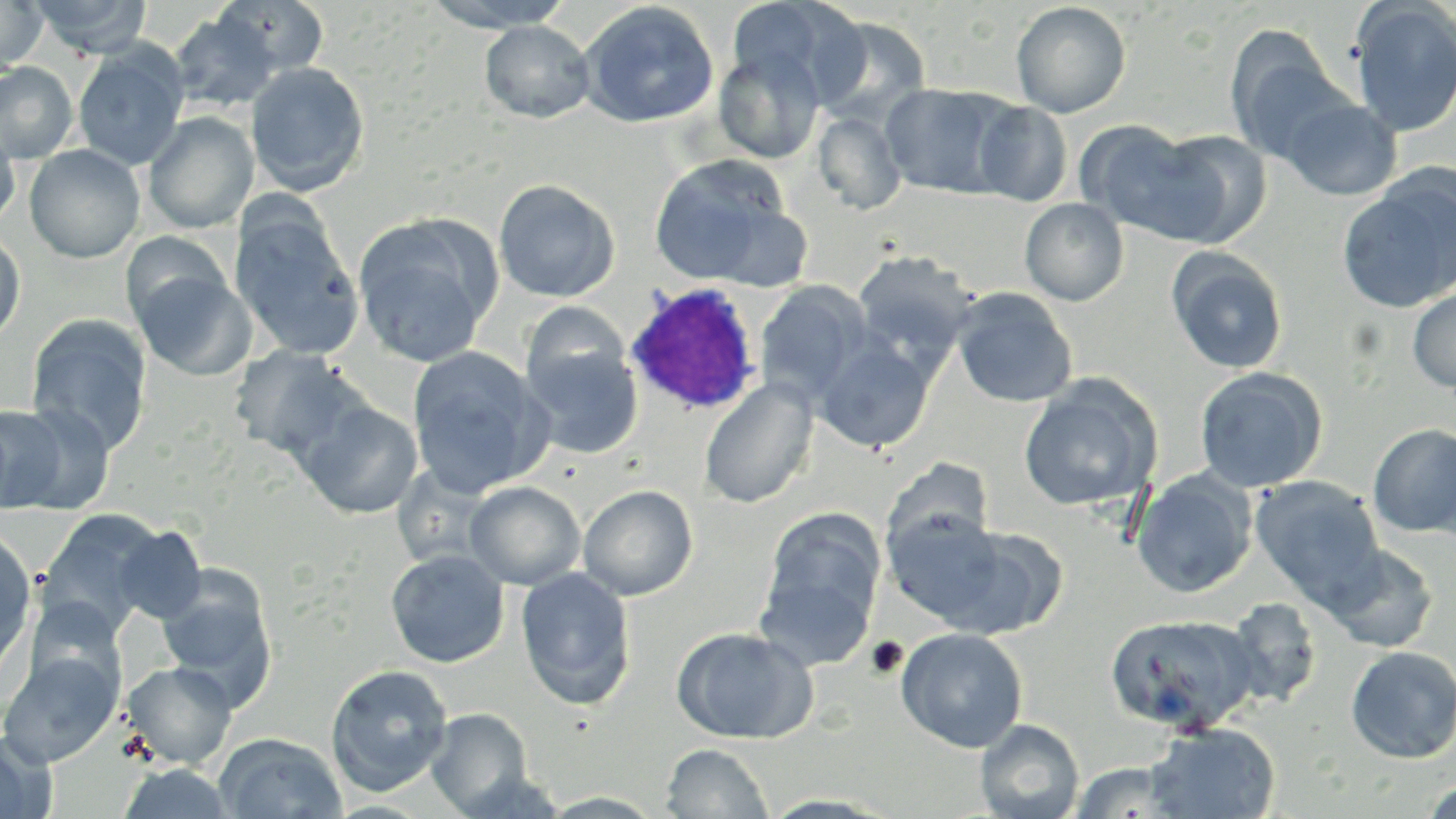
slide_level_diagnosis: Plasmodium ovale
image_size: 1456×819 pixels
uninfected_red_blood_cell_locations: 'approximate bounding boxes as (x1,y1)-(x2,y2) corner pairs in pixels: (30,0)-(152,58), (215,0)-(329,78), (426,0)-(573,31), (727,0)-(840,93), (0,1)-(47,72), (578,1)-(720,129), (1349,1)-(1456,138), (1011,2)-(1131,118), (169,11)-(281,113), (815,15)-(933,122), (480,21)-(595,123), (1224,29)-(1347,166), (73,44)-(189,171), (713,47)-(825,164), (0,62)-(78,163), (245,62)-(370,196), (880,83)-(1014,199), (1278,96)-(1402,201), (972,101)-(1073,206), (143,111)-(259,234), (813,111)-(907,215), (1074,120)-(1208,238), (0,122)-(21,232), (1144,128)-(1272,248), (24,144)-(145,263), (648,156)-(790,285), (1337,170)-(1456,313), (494,179)-(620,302), (1020,198)-(1129,306), (702,203)-(813,292), (229,207)-(364,360), (352,214)-(501,367), (0,228)-(25,347), (120,231)-(234,332), (1166,248)-(1288,374), (851,250)-(978,371), (130,263)-(255,381), (755,282)-(871,405), (1407,287)-(1456,394), (950,288)-(1078,408), (521,301)-(632,399), (26,315)-(153,457), (521,337)-(645,460), (815,337)-(936,453), (227,345)-(362,461), (406,346)-(551,497), (1193,366)-(1328,493), (699,377)-(818,509), (1018,377)-(1162,513), (297,400)-(424,519), (3,401)-(115,515), (1368,424)-(1456,539), (883,457)-(994,553), (1132,470)-(1257,598), (1250,476)-(1384,606), (464,481)-(586,590), (578,484)-(698,601), (882,507)-(1008,627), (38,509)-(168,636), (756,512)-(885,664), (112,525)-(207,624), (938,526)-(1067,639), (0,530)-(38,675), (1323,542)-(1439,653), (385,549)-(510,668), (515,566)-(637,709), (156,574)-(277,708), (1222,597)-(1322,710), (1105,611)-(1260,735), (671,625)-(818,744), (895,627)-(1028,753), (1345,645)-(1456,764), (1,648)-(122,766), (123,660)-(237,768), (325,663)-(453,797), (425,707)-(533,816), (975,718)-(1084,819), (1145,723)-(1281,819), (0,733)-(56,819), (215,733)-(347,818), (660,742)-(773,819), (1071,760)-(1181,818), (118,762)-(236,819), (1419,778)-(1456,819)'
stain: May-Grünwald-Giemsa
modality: optical microscopy
platelet_locations: 'approximate bounding boxes as (x1,y1)-(x2,y2) corner pairs in pixels: (863,636)-(909,681)'
white_blood_cell_locations: 'approximate bounding boxes as (x1,y1)-(x2,y2) corner pairs in pixels: (625,280)-(764,417)'
field_of_view: single
magnification: 1000x
preparation: thin blood film